Name the cell type shown.
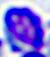
This is a leukocyte.

Photomicrograph. Captured at 400x magnification.